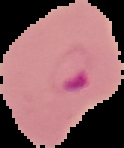 The area outside the segmented cell region is set to black. Image is 124×148 pixels. Malaria status: parasitized. From a thin blood smear.